Classify this cell by malaria status.
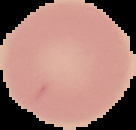
It is uninfected.

Summary:
  - Image size: 136×130 pixels
  - Image type: segmented cell region with the area outside set to black
  - Preparation: thin blood film